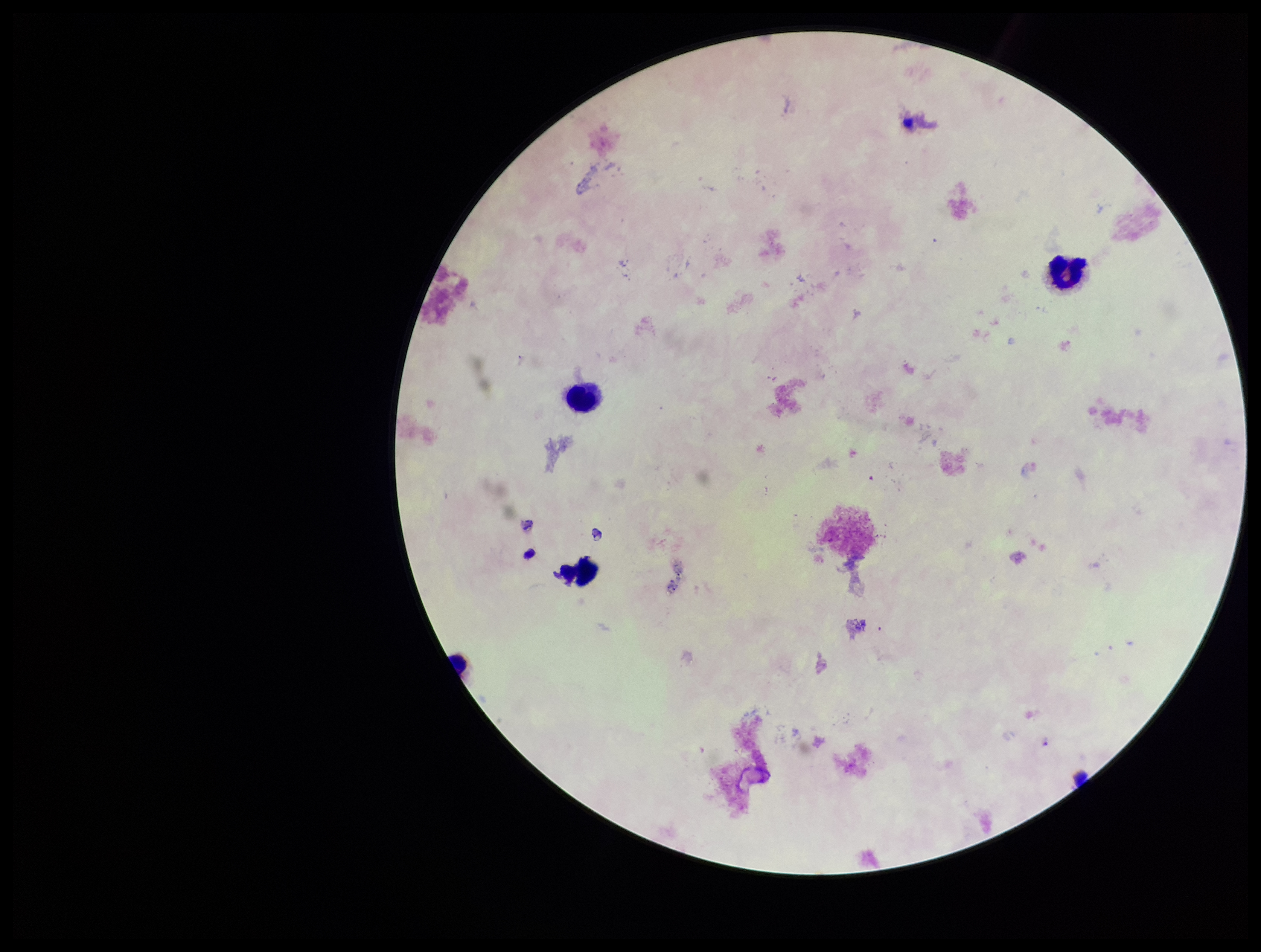
plasmodium_parasites: none detected
capture: smartphone photograph through the microscope eyepiece
preparation: thick smear
leukocyte_count: 3
species_reported_for_this_patient: Plasmodium falciparum
parasite_count: 0
image_size: 1261×952 pixels
field_of_view: one from this slide
stain: Giemsa
patient_malaria_status: infected